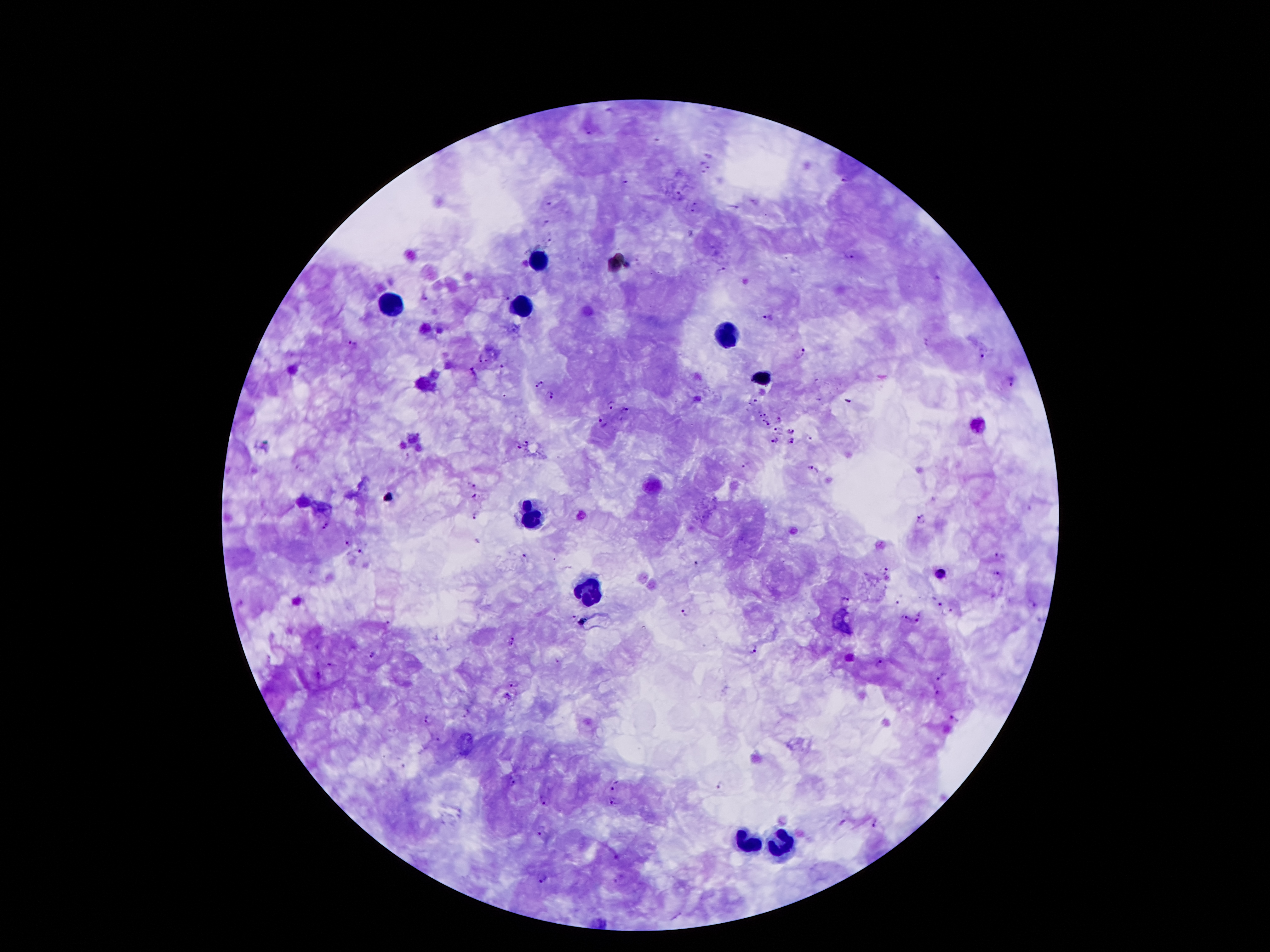
Approximate object centers, in pixels from the top-left corner. Leukocyte locations: (x=539, y=260), (x=393, y=304), (x=523, y=307), (x=730, y=334), (x=764, y=374), (x=533, y=517), (x=590, y=594), (x=744, y=840), (x=778, y=844). Plasmodium parasite locations: (x=590, y=133), (x=711, y=156), (x=709, y=166), (x=702, y=172), (x=847, y=179), (x=626, y=183), (x=682, y=196), (x=697, y=203), (x=548, y=204), (x=735, y=206), (x=693, y=211), (x=545, y=221), (x=548, y=241), (x=851, y=257), (x=723, y=268), (x=938, y=276), (x=507, y=296), (x=425, y=299), (x=768, y=317), (x=354, y=342), (x=982, y=355), (x=479, y=356), (x=801, y=356), (x=487, y=361), (x=503, y=366), (x=473, y=370), (x=1012, y=381), (x=541, y=382), (x=535, y=388), (x=552, y=396), (x=753, y=401), (x=847, y=401), (x=610, y=404), (x=625, y=409), (x=766, y=413), (x=779, y=419), (x=762, y=420), (x=603, y=421), (x=768, y=422), (x=777, y=429), (x=790, y=430), (x=810, y=437), (x=775, y=441), (x=791, y=441), (x=526, y=442), (x=518, y=447), (x=746, y=465), (x=810, y=467), (x=472, y=486), (x=473, y=496), (x=476, y=514), (x=920, y=519), (x=325, y=526), (x=348, y=542), (x=361, y=550), (x=1001, y=554), (x=522, y=555), (x=553, y=559), (x=697, y=562), (x=886, y=568), (x=997, y=572), (x=942, y=574), (x=845, y=599), (x=936, y=599), (x=898, y=602), (x=1034, y=605), (x=685, y=611), (x=949, y=612), (x=574, y=616), (x=920, y=616), (x=906, y=619), (x=389, y=622), (x=514, y=641), (x=754, y=649), (x=371, y=655), (x=558, y=661), (x=880, y=663), (x=332, y=664), (x=319, y=675), (x=940, y=675), (x=515, y=685), (x=937, y=692), (x=508, y=698), (x=467, y=714), (x=427, y=719), (x=955, y=719), (x=438, y=739), (x=515, y=782), (x=721, y=784), (x=615, y=785), (x=546, y=801), (x=613, y=803), (x=843, y=822), (x=876, y=826), (x=541, y=833), (x=615, y=858), (x=543, y=879), (x=616, y=882). Patient malaria status: infected with Plasmodium falciparum. Photographed through the microscope eyepiece with a smartphone camera. 100x magnification. Single field of view. Image is 1270×952 pixels. Giemsa stain. Thick blood smear.